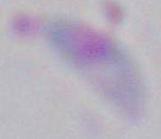
Summary:
  - Modality: micrograph
  - Identification: Toxoplasma gondii
  - Magnification: 1000x